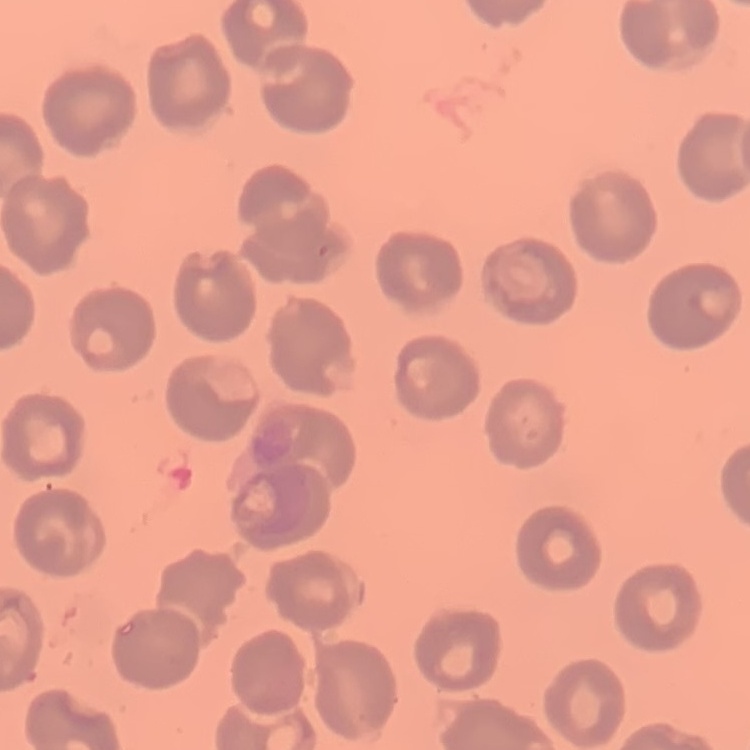

Summary:
  - Red blood cell morphology: no rouleaux formation
  - Preparation: thin peripheral smear
  - Stain: Field's or Giemsa
  - Image type: square crop of a larger photomicrograph